Report the malaria status of this cell.
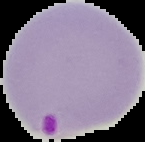
It is parasitized.

Summary:
  - Image type: cell region segmented out of the field of view; surrounding area masked to black
  - Image size: 145×142 pixels
  - Preparation: thin blood film